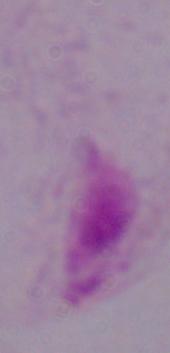

{
  "magnification": "1000x",
  "identification": "trichomonad",
  "modality": "micrograph"
}